Outline each blood parasite and name the species.
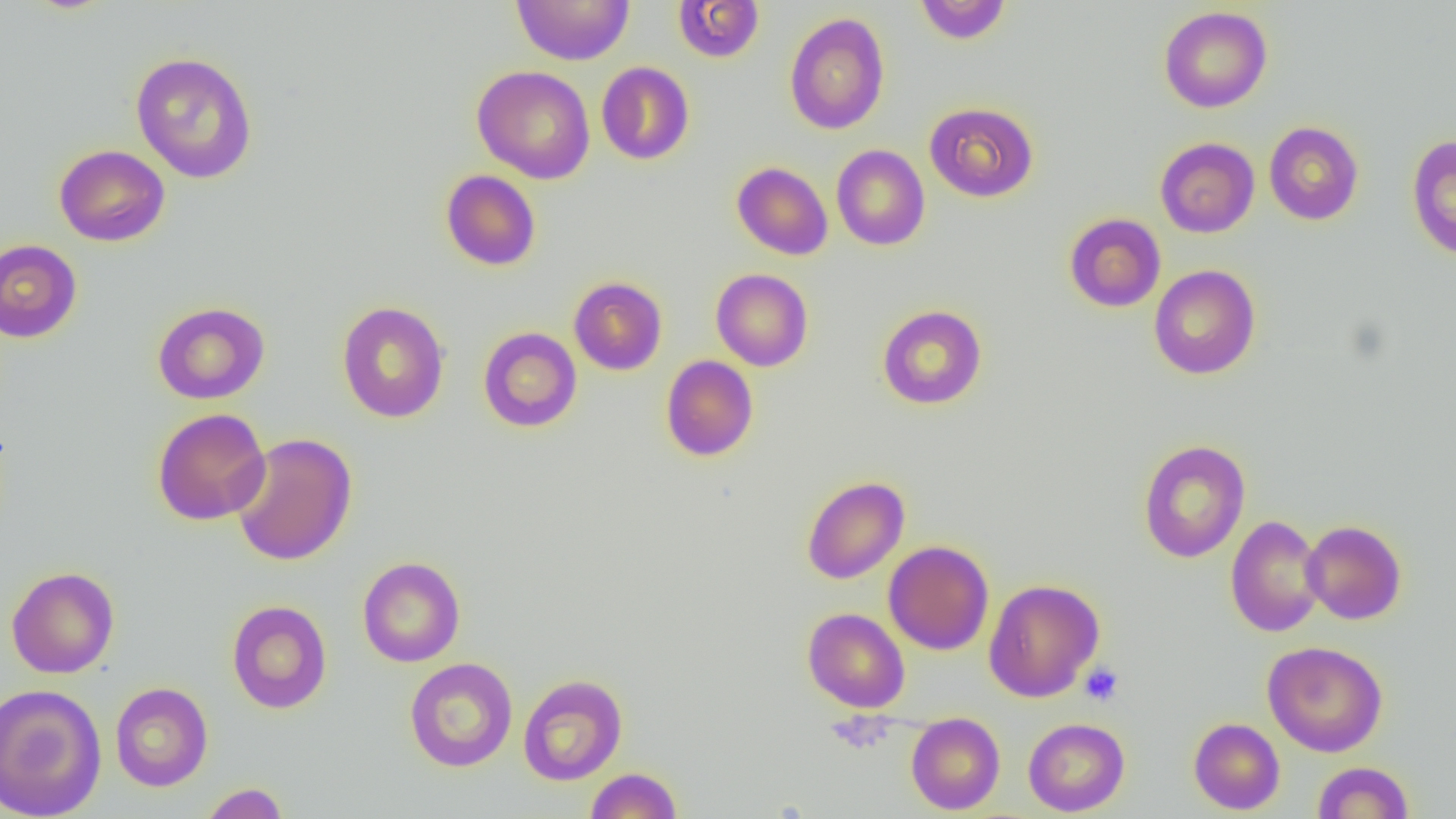
No blood parasites seen.

Summary:
  - Coordinate format: approximate bounding boxes as (x1,y1)-(x2,y2) corner pairs in pixels
  - Platelet locations: (1079,662)-(1124,706)
  - Uninfected red blood cell locations: (511,0)-(634,65), (914,0)-(1012,44), (672,1)-(764,63), (1158,6)-(1273,113), (784,12)-(890,135), (130,51)-(258,183), (596,61)-(695,165), (472,65)-(595,184), (924,102)-(1039,202), (1263,121)-(1364,225), (1405,134)-(1456,261), (1155,137)-(1260,238), (54,144)-(170,247), (831,145)-(930,250), (732,162)-(833,260), (440,170)-(541,271), (1064,213)-(1166,312), (0,238)-(82,343), (1149,264)-(1260,380), (711,268)-(813,371), (569,276)-(667,375), (337,301)-(449,423), (152,302)-(269,404), (877,304)-(987,409), (478,327)-(582,432), (661,355)-(758,462), (152,407)-(271,525), (230,432)-(358,566), (1137,439)-(1250,563), (801,476)-(909,584), (1225,515)-(1326,637), (1301,520)-(1407,625), (883,540)-(994,655), (357,556)-(465,667), (6,566)-(120,678), (984,578)-(1104,702), (226,600)-(332,714), (802,607)-(910,712), (1263,641)-(1388,757), (405,657)-(518,772), (518,674)-(628,785), (111,682)-(213,792), (0,683)-(107,819), (906,712)-(1005,814), (1023,717)-(1130,816), (1188,717)-(1285,815), (1311,761)-(1415,818), (585,767)-(683,819), (198,782)-(290,819)
  - Slide-level diagnosis: no evidence of blood parasites
  - Modality: optical microscopy
  - Image size: 1456×819 pixels
  - Field of view: single
  - Preparation: thin blood film
  - Magnification: 1000x